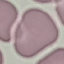
Summary:
  - Malaria status: uninfected
  - Capture: smartphone camera at the microscope eyepiece
  - Stain: Giemsa
  - Preparation: thin blood smear
  - Image type: automatically extracted cell patch, resized to 64 × 64 pixels